Classify the preparation.
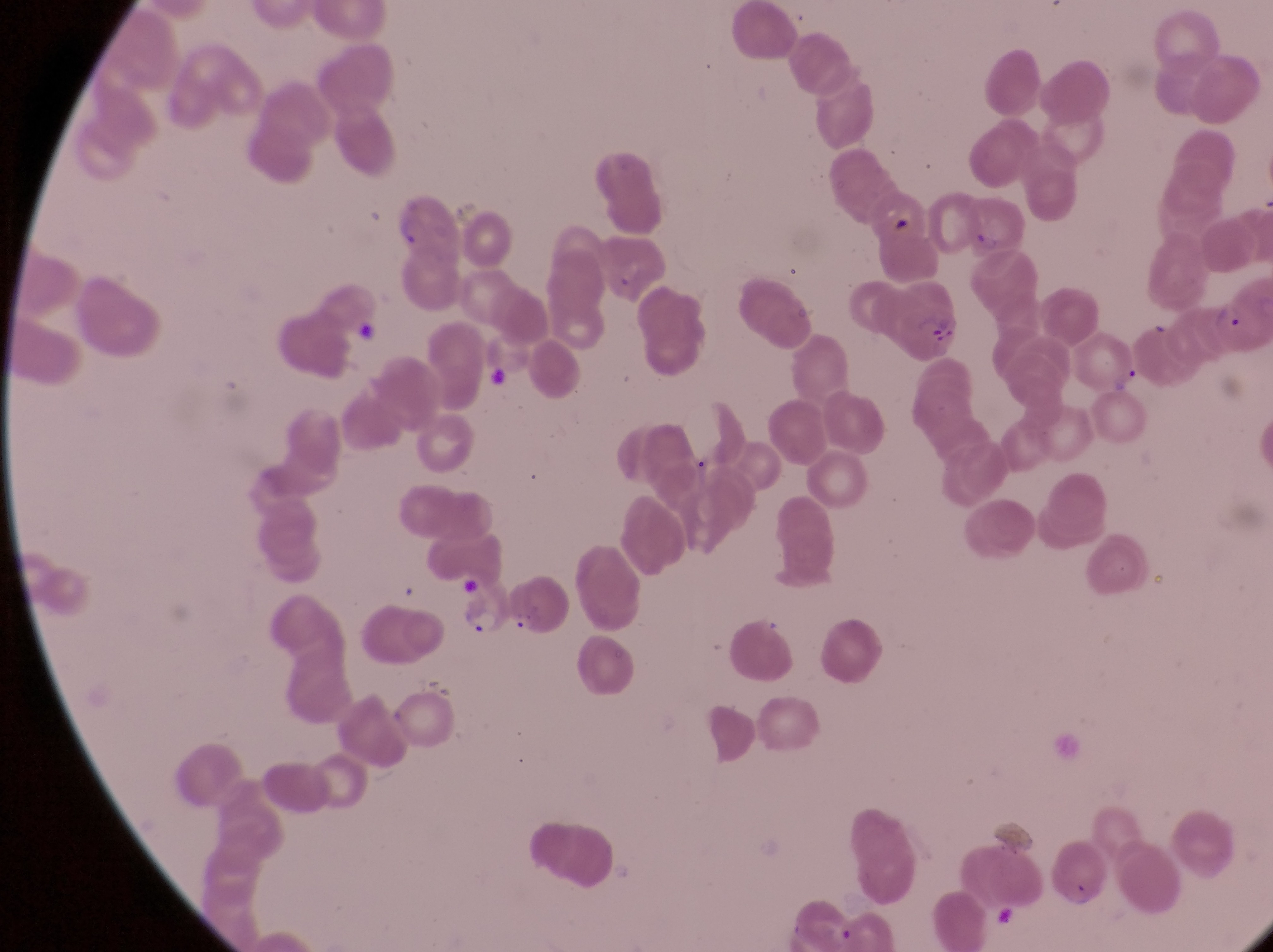

This is a thin smear.

Approximate bounding boxes as {left, top, right, bottom} in pixels.
Summary:
  - Trophozoite locations: {460, 602, 502, 637}
  - Parasitised red blood cell locations: {963, 185, 1026, 255}, {599, 232, 664, 299}, {863, 270, 965, 358}
  - Artifact (platelet-like body, stain precipitate, or debris) locations: {886, 207, 921, 234}, {352, 317, 385, 352}, {1126, 354, 1153, 394}, {477, 359, 522, 396}
  - Country: Uganda
  - Capture: smartphone photograph through the eyepiece of an Olympus CX-23 microscope
  - Image size: 1273×952 pixels
  - Field of view: single
  - Magnification: 1000x